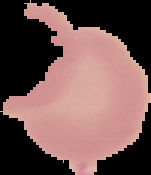

Image is 151×175 pixels. Result: negative for malaria parasites. From a thin blood smear. Cell region segmented out of the field of view; the surrounding area is masked to black.